Comment on the morphology of the red blood cells.
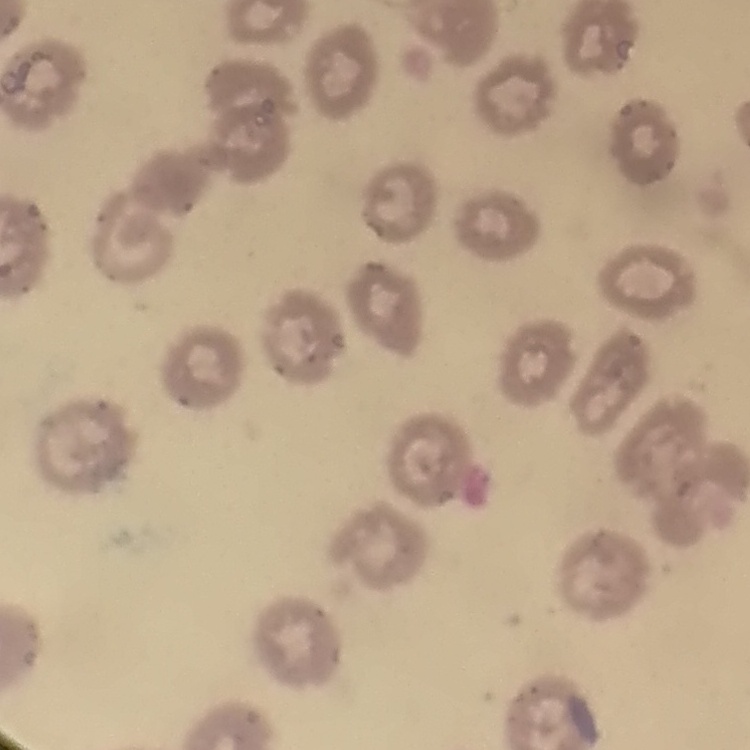
They show no rouleaux formation.

preparation = thin peripheral smear
stain = Field's or Giemsa
image type = square crop of a larger photomicrograph